Identify the blood parasite species.
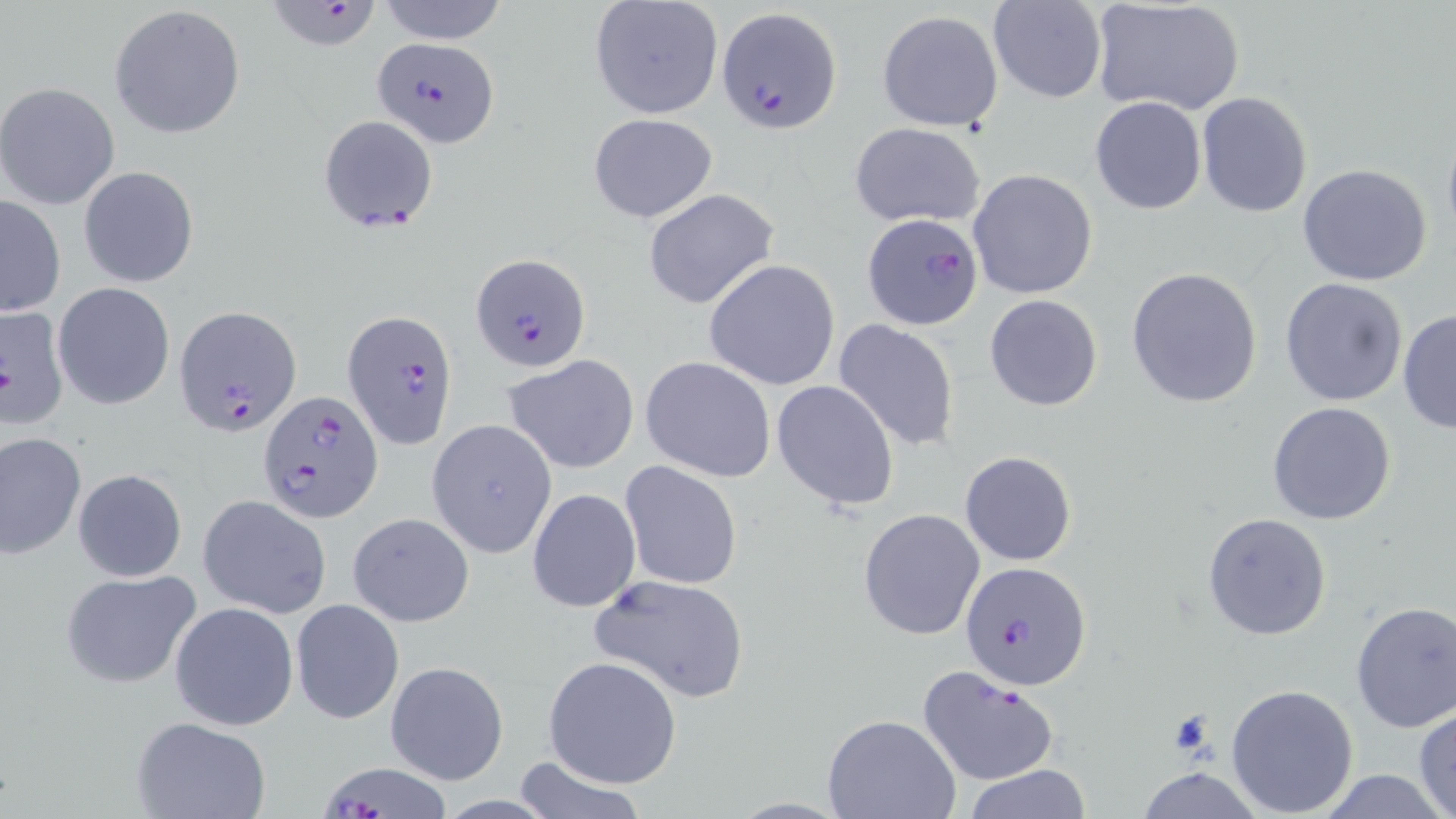
Plasmodium falciparum.

Approximate bounding boxes as (x1,y1)-(x2,y2) corner pairs in pixels. Uninfected red blood cell locations: (376,0)-(510,45), (588,0)-(725,120), (988,1)-(1108,103), (1090,1)-(1245,116), (109,4)-(246,140), (877,9)-(1005,131), (0,83)-(120,210), (1196,93)-(1312,216), (1089,95)-(1206,213), (587,112)-(719,223), (1440,118)-(1456,251), (849,122)-(985,228), (1296,163)-(1433,286), (79,165)-(199,288), (968,168)-(1098,299), (643,188)-(778,310), (1,195)-(66,316), (704,258)-(841,390), (1125,266)-(1263,408), (1279,277)-(1408,407), (53,283)-(176,410), (984,295)-(1103,410), (1397,308)-(1456,434), (833,318)-(961,453), (503,356)-(641,474), (641,357)-(776,482), (771,379)-(900,511), (1267,401)-(1398,526), (427,418)-(558,559), (1,432)-(85,558), (960,451)-(1076,566), (619,460)-(743,589), (72,468)-(187,582), (526,487)-(641,612), (197,493)-(331,618), (858,507)-(985,641), (347,511)-(475,628), (1202,513)-(1332,641), (60,568)-(202,688), (590,572)-(750,703), (291,599)-(404,724), (170,601)-(298,731), (1349,601)-(1456,732), (543,656)-(682,788), (385,660)-(508,785), (1226,682)-(1359,816), (1413,706)-(1456,819), (825,715)-(961,819), (133,716)-(273,819), (511,756)-(646,819), (964,763)-(1092,818), (1135,766)-(1265,819), (1316,768)-(1448,819), (727,798)-(853,818). Plasmodium falciparum-infected red blood cell locations: (275,4)-(390,54), (719,6)-(841,133), (372,35)-(501,147), (317,115)-(439,232), (862,214)-(983,329), (471,252)-(589,373), (175,306)-(302,437), (0,307)-(70,431), (343,308)-(460,450), (257,391)-(381,522), (963,560)-(1093,688), (917,664)-(1059,788), (324,760)-(446,819). Image is 1456×819 pixels. May-Grünwald-Giemsa-stained preparation. One field of a larger specimen. Thin blood smear. Optical microscopy. 1000x magnification.